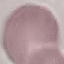

result = no malaria parasites seen
image type = automatically extracted cell patch, resized to 64 × 64 pixels
capture = smartphone through the microscope eyepiece
stain = Giemsa
preparation = thin blood film